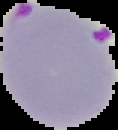
Summary:
  - Image type: cell region segmented out of the field of view; surrounding area masked to black
  - Image size: 118×130 pixels
  - Preparation: thin blood film
  - Result: Plasmodium parasites identified